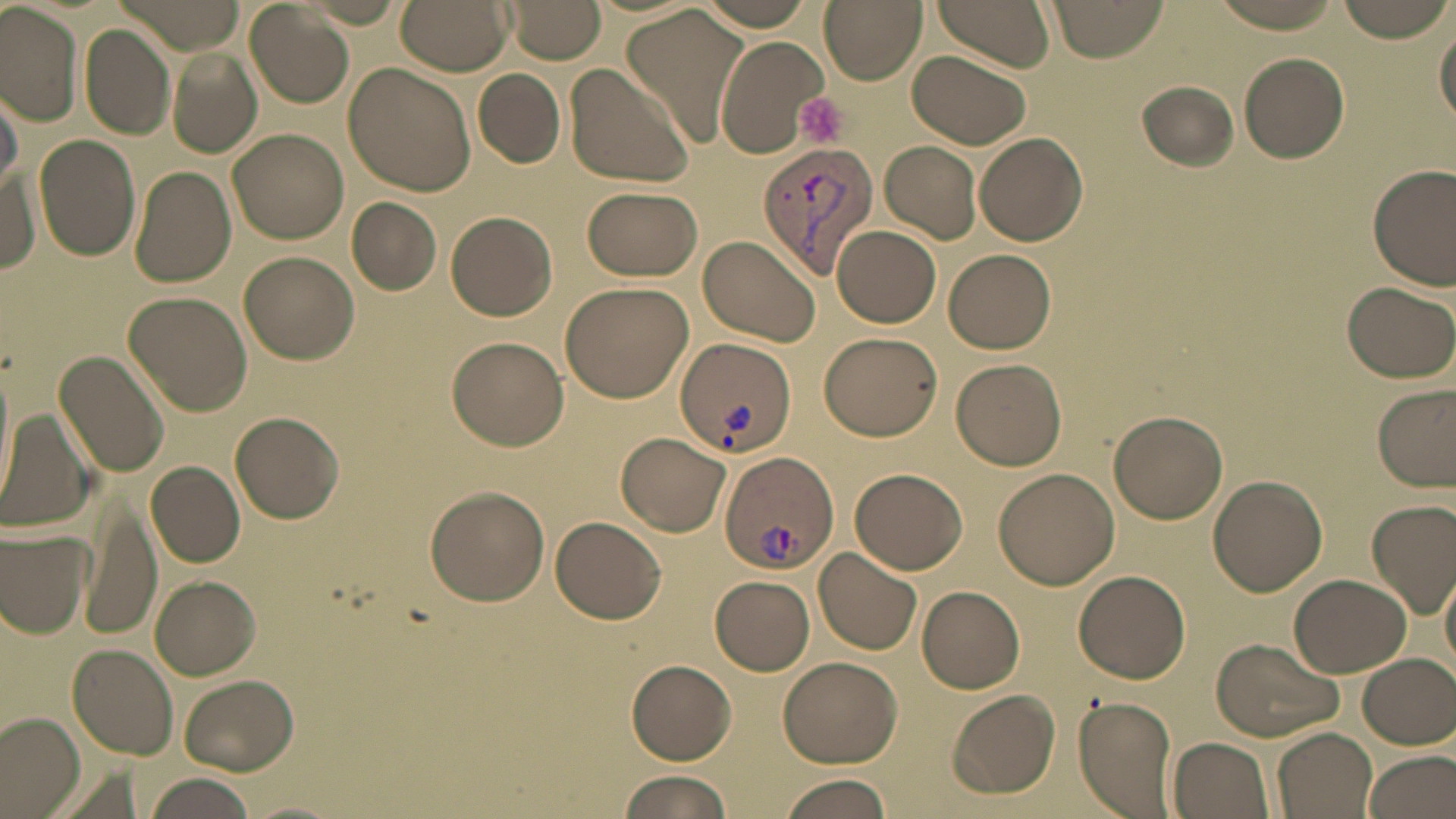

Approximate bounding boxes as (x1,y1)-(x2,y2) corner pairs in pixels. Platelet locations: (794,93)-(847,147). Uninfected red blood cell locations: (394,0)-(514,74), (819,0)-(927,84), (933,0)-(1058,70), (1046,0)-(1170,61), (1206,0)-(1348,31), (1338,0)-(1452,43), (112,1)-(242,54), (506,1)-(607,65), (0,3)-(82,127), (245,3)-(355,108), (622,4)-(751,140), (1435,15)-(1456,129), (79,24)-(175,140), (713,34)-(830,157), (908,47)-(1036,150), (168,52)-(261,158), (1238,52)-(1351,163), (561,62)-(696,188), (342,63)-(476,196), (473,70)-(565,168), (1138,80)-(1238,171), (0,85)-(22,196), (227,127)-(349,244), (972,133)-(1088,246), (35,134)-(140,261), (881,141)-(981,244), (1368,164)-(1455,290), (128,166)-(236,288), (2,172)-(40,272), (582,187)-(702,280), (347,199)-(442,294), (445,210)-(557,320), (831,224)-(941,328), (696,235)-(821,347), (944,249)-(1056,354), (238,252)-(358,365), (560,279)-(696,403), (1339,281)-(1456,383), (123,291)-(253,416), (817,331)-(942,440), (448,336)-(568,450), (53,348)-(171,478), (0,357)-(15,506), (951,358)-(1067,470), (1372,382)-(1455,492), (0,409)-(93,533), (1110,411)-(1227,524), (231,412)-(344,524), (617,433)-(729,536), (145,461)-(244,569), (847,467)-(970,575), (993,467)-(1121,590), (1207,475)-(1327,595), (424,484)-(550,606), (81,494)-(160,640), (1365,497)-(1456,618), (550,513)-(668,624), (0,525)-(93,638), (814,547)-(922,655), (1440,557)-(1456,679), (1071,569)-(1191,683), (1289,573)-(1412,678), (152,574)-(261,678), (709,575)-(815,675), (917,585)-(1025,693), (1210,638)-(1346,743), (67,644)-(178,761), (1356,653)-(1456,750), (777,655)-(902,768), (627,659)-(737,764), (177,673)-(300,775), (947,690)-(1060,799), (1072,695)-(1179,819), (0,712)-(86,817), (1271,728)-(1378,819), (1167,736)-(1276,819), (1364,749)-(1456,819), (617,770)-(732,819), (143,774)-(259,818), (775,774)-(896,819). Plasmodium vivax-infected red blood cell locations: (757,139)-(879,281), (674,337)-(796,459), (717,450)-(839,576). Slide-level diagnosis: Plasmodium vivax. Light microscopy. Thin blood film. May-Grünwald-Giemsa-stained preparation. One field of a larger specimen. Captured at 1000x magnification. Image is 1456×819 pixels.